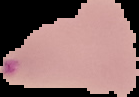
Malaria status: parasitized. Image is 139×97 pixels. From a thin blood smear. Segmented cell region on a black background.